Locate every Plasmodium falciparum-infected red blood cell.
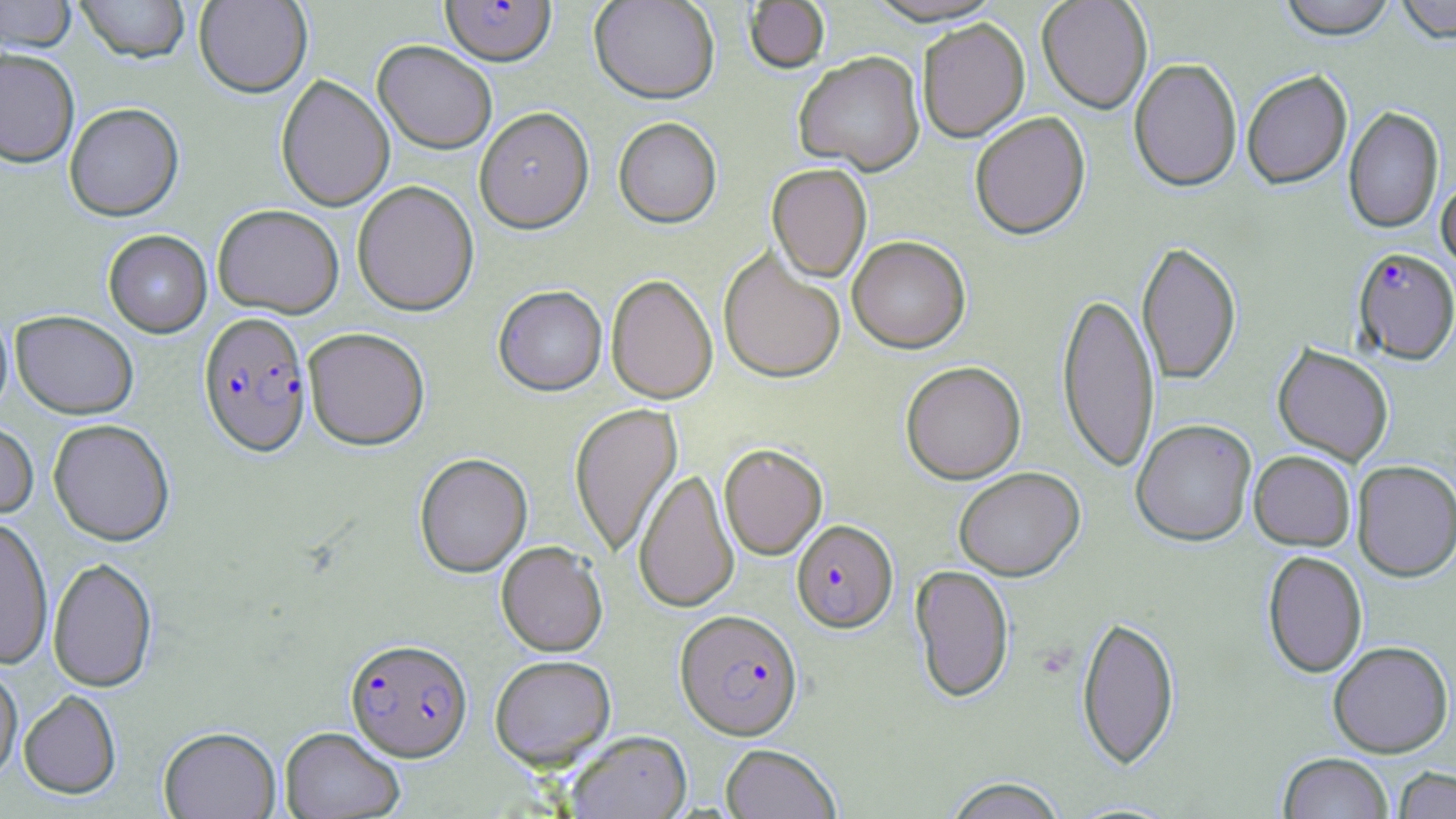

Approximate bounding boxes as (x1, y1, x2, y2) in pixels.
Plasmodium falciparum-infected red blood cells: (440, 1, 556, 68), (1352, 250, 1456, 368), (198, 312, 312, 457), (791, 521, 898, 635), (674, 611, 803, 742), (345, 638, 473, 762).

Summary:
  - Uninfected red blood cell locations: (0, 0, 77, 53), (75, 0, 191, 64), (194, 0, 312, 98), (589, 0, 719, 105), (863, 0, 1008, 29), (1036, 0, 1152, 116), (1278, 0, 1396, 44), (1396, 0, 1456, 48), (744, 1, 830, 75), (918, 21, 1030, 145), (372, 41, 497, 154), (0, 48, 80, 167), (793, 54, 926, 178), (1129, 60, 1242, 195), (1242, 72, 1353, 192), (276, 74, 394, 212), (64, 103, 184, 222), (1343, 107, 1444, 236), (474, 108, 594, 235), (970, 115, 1091, 242), (613, 119, 722, 230), (766, 165, 872, 284), (1436, 175, 1456, 279), (352, 181, 479, 316), (213, 204, 344, 319), (103, 230, 212, 338), (847, 238, 970, 355), (1136, 244, 1241, 387), (718, 249, 845, 385), (606, 275, 717, 405), (494, 286, 607, 396), (1056, 291, 1160, 475), (0, 306, 13, 419), (11, 310, 138, 419), (303, 327, 430, 450), (1272, 345, 1393, 467), (900, 363, 1027, 486), (569, 403, 682, 558), (48, 419, 175, 546), (0, 421, 38, 520), (1131, 421, 1256, 549), (719, 444, 828, 560), (1249, 452, 1355, 552), (414, 453, 532, 578), (1352, 462, 1456, 585), (634, 469, 739, 614), (954, 469, 1085, 583), (0, 516, 54, 669), (496, 542, 607, 657), (1262, 553, 1367, 679), (47, 557, 158, 692), (910, 565, 1014, 704), (1076, 617, 1180, 771), (1328, 643, 1453, 760), (490, 655, 616, 770), (0, 662, 23, 782), (19, 690, 121, 799), (159, 726, 281, 819), (279, 727, 404, 819), (565, 731, 692, 819), (720, 744, 841, 819), (1278, 754, 1393, 819), (1393, 767, 1456, 819), (943, 777, 1068, 819)
  - Slide-level diagnosis: Plasmodium falciparum
  - Preparation: thin blood smear
  - Stain: May-Grünwald-Giemsa
  - Image size: 1456×819 pixels
  - Magnification: 1000x
  - Modality: light microscopy
  - Field of view: one of a larger specimen